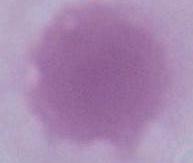

A red blood cell is shown. Photomicrograph. 1000x magnification.